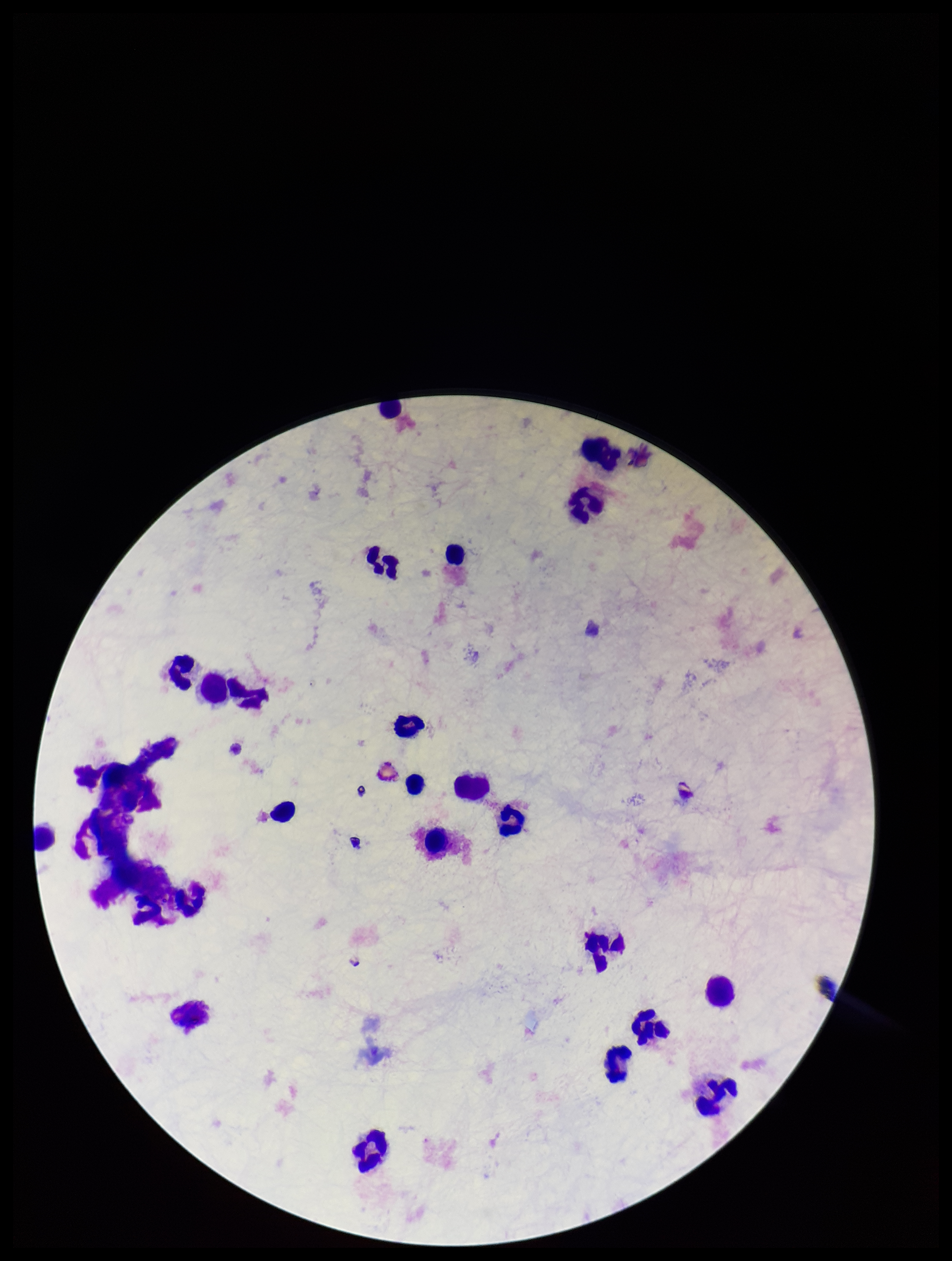
Summary:
  - Field of view: one from this slide
  - Stain: Giemsa
  - Plasmodium parasites: none identified
  - Preparation: thick blood smear
  - Image size: 952×1261 pixels
  - Leukocyte count: 24
  - Parasite count: 0
  - Capture: smartphone photograph through the microscope eyepiece
  - Patient malaria status: negative